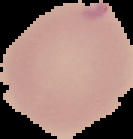

Summary:
  - Preparation: thin blood film
  - Image size: 133×139 pixels
  - Image type: segmented cell region with the area outside set to black
  - Result: no Plasmodium parasites seen